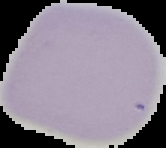
Malaria status: uninfected. Cell region segmented out of the field of view; the surrounding area is masked to black. From a thin blood film. Image is 166×148 pixels.